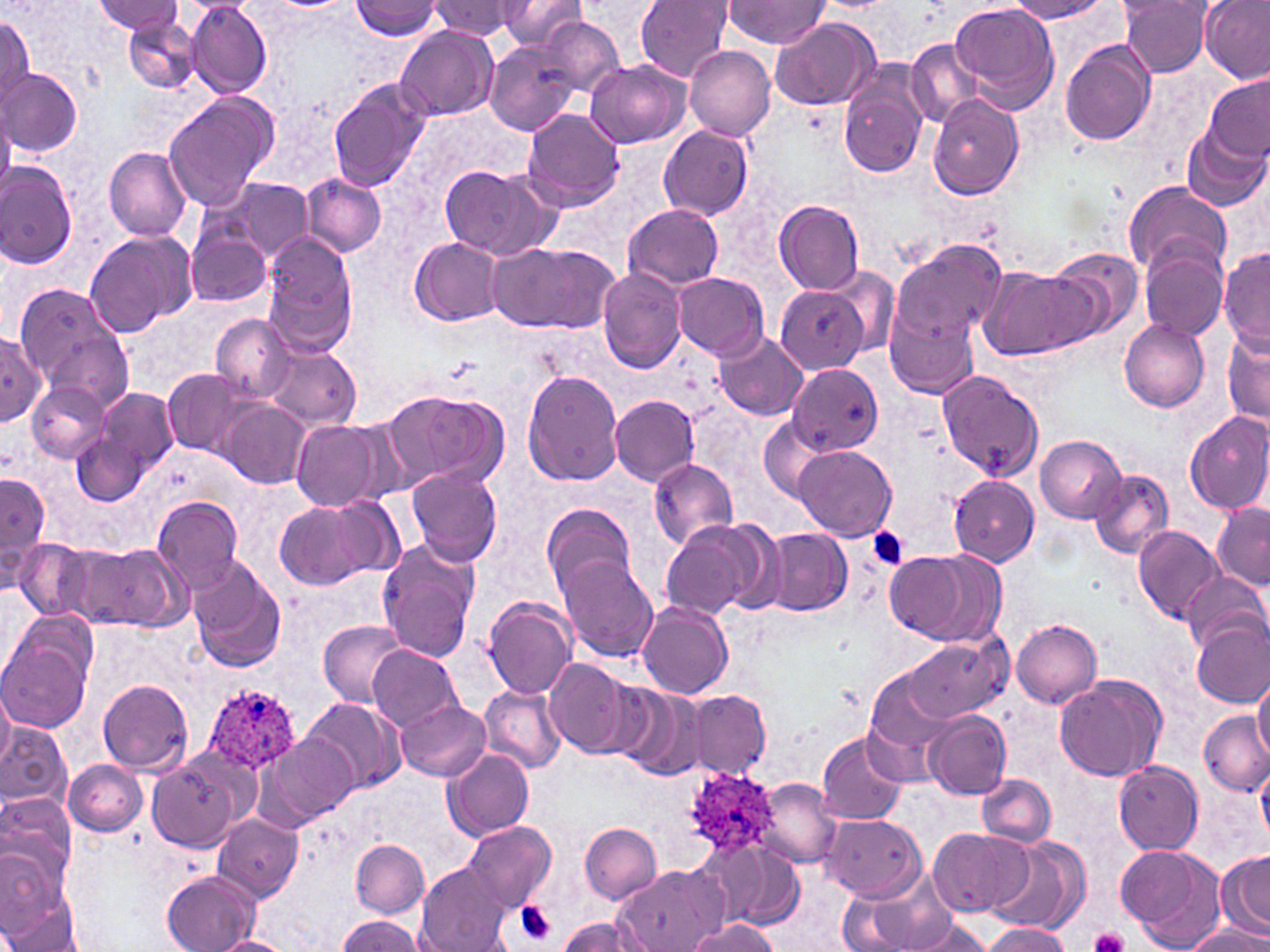
{
  "slide_level_diagnosis": "Plasmodium ovale",
  "magnification": "1000x",
  "field_of_view": "single",
  "preparation": "thin blood smear",
  "plasmodium_ovale_infected_red_blood_cell_locations": "approximate bounding boxes as (x1,y1)-(x2,y2) corner pairs in pixels: (201,683)-(300,774), (682,769)-(775,864)",
  "stain": "May-Grünwald-Giemsa",
  "uninfected_red_blood_cell_locations": "approximate bounding boxes as (x1,y1)-(x2,y2) corner pairs in pixels: (94,0)-(184,36), (496,0)-(588,52), (636,0)-(734,82), (1006,0)-(1108,22), (1198,0)-(1269,84), (350,1)-(442,39), (429,1)-(519,39), (1121,1)-(1214,77), (723,2)-(831,48), (949,2)-(1060,111), (186,3)-(272,100), (124,16)-(204,94), (0,17)-(34,108), (769,17)-(880,112), (540,19)-(624,96), (393,26)-(497,121), (1060,39)-(1157,147), (907,41)-(982,126), (484,43)-(578,135), (683,45)-(776,142), (584,60)-(691,149), (2,67)-(83,156), (837,67)-(929,177), (1203,74)-(1269,161), (327,79)-(430,192), (162,93)-(278,212), (928,95)-(1024,201), (0,107)-(14,203), (520,108)-(626,212), (1180,123)-(1269,213), (658,124)-(752,221), (104,146)-(192,241), (438,162)-(559,260), (0,165)-(77,268), (300,173)-(387,258), (202,177)-(315,264), (1122,180)-(1232,281), (772,200)-(865,293), (623,204)-(724,290), (187,227)-(274,308), (84,231)-(197,336), (262,236)-(357,352), (409,237)-(504,324), (889,240)-(1007,347), (487,241)-(618,334), (1139,246)-(1228,342), (1044,248)-(1143,338), (1218,248)-(1269,353), (830,265)-(901,357), (980,267)-(1098,357), (598,269)-(688,376), (674,272)-(770,361), (15,284)-(124,386), (776,285)-(868,373), (885,310)-(978,399), (212,314)-(293,401), (1119,320)-(1210,412), (1,329)-(49,422), (43,329)-(131,416), (714,333)-(808,420), (1222,333)-(1270,424), (262,344)-(362,430), (788,366)-(885,455), (162,368)-(253,457), (523,369)-(625,486), (937,372)-(1043,480), (27,382)-(107,463), (92,385)-(179,482), (385,390)-(509,492), (610,395)-(700,486), (221,401)-(310,488), (1185,412)-(1270,514), (759,415)-(836,503), (291,420)-(384,510), (72,423)-(151,507), (1035,433)-(1130,523), (793,445)-(896,541), (648,458)-(738,549), (406,465)-(503,568), (1088,468)-(1173,561), (1,472)-(50,586), (947,474)-(1039,566), (151,494)-(245,590), (274,498)-(387,591), (541,502)-(640,602), (1211,502)-(1269,590), (660,520)-(772,622), (1133,525)-(1226,627), (764,529)-(852,616), (13,537)-(95,620), (377,537)-(482,662), (90,542)-(190,632), (883,545)-(996,642), (559,555)-(657,662), (188,556)-(286,673), (1181,573)-(1269,655), (483,598)-(577,699), (637,602)-(733,699), (1010,616)-(1102,708), (318,620)-(407,705), (1192,620)-(1270,707), (0,629)-(94,732), (903,634)-(1009,723), (367,644)-(461,731), (545,658)-(640,757), (865,669)-(961,770), (1055,673)-(1166,781), (1253,673)-(1270,762), (97,678)-(195,774), (612,685)-(706,781), (479,686)-(566,774), (686,690)-(771,778), (0,695)-(14,773), (302,697)-(406,795), (395,701)-(489,781), (923,711)-(1010,801), (1200,711)-(1268,797), (0,723)-(73,814), (816,730)-(908,824), (261,733)-(356,829), (442,747)-(534,842), (155,755)-(269,924), (148,757)-(243,851), (64,760)-(148,835), (1114,760)-(1204,854), (1257,764)-(1270,844), (978,773)-(1055,846), (756,778)-(842,866), (0,793)-(77,897), (212,813)-(304,901), (821,814)-(925,901), (464,821)-(557,914), (580,822)-(662,903), (927,826)-(1032,918), (987,835)-(1090,934), (351,839)-(429,918), (1116,843)-(1222,944), (720,848)-(803,930), (1219,852)-(1270,936), (617,864)-(725,952), (415,865)-(515,951), (843,865)-(958,952), (0,868)-(81,952), (162,871)-(260,951), (336,914)-(424,952), (904,915)-(996,952), (558,916)-(649,952), (690,919)-(782,951), (980,923)-(1071,952), (1183,925)-(1270,951), (211,936)-(292,952)",
  "image_size": "1270×952 pixels",
  "platelet_locations": "approximate bounding boxes as (x1,y1)-(x2,y2) corner pairs in pixels: (867,527)-(909,569), (515,901)-(556,945), (1091,927)-(1130,952)",
  "modality": "light microscopy"
}